Outline each Trypanosoma brucei.
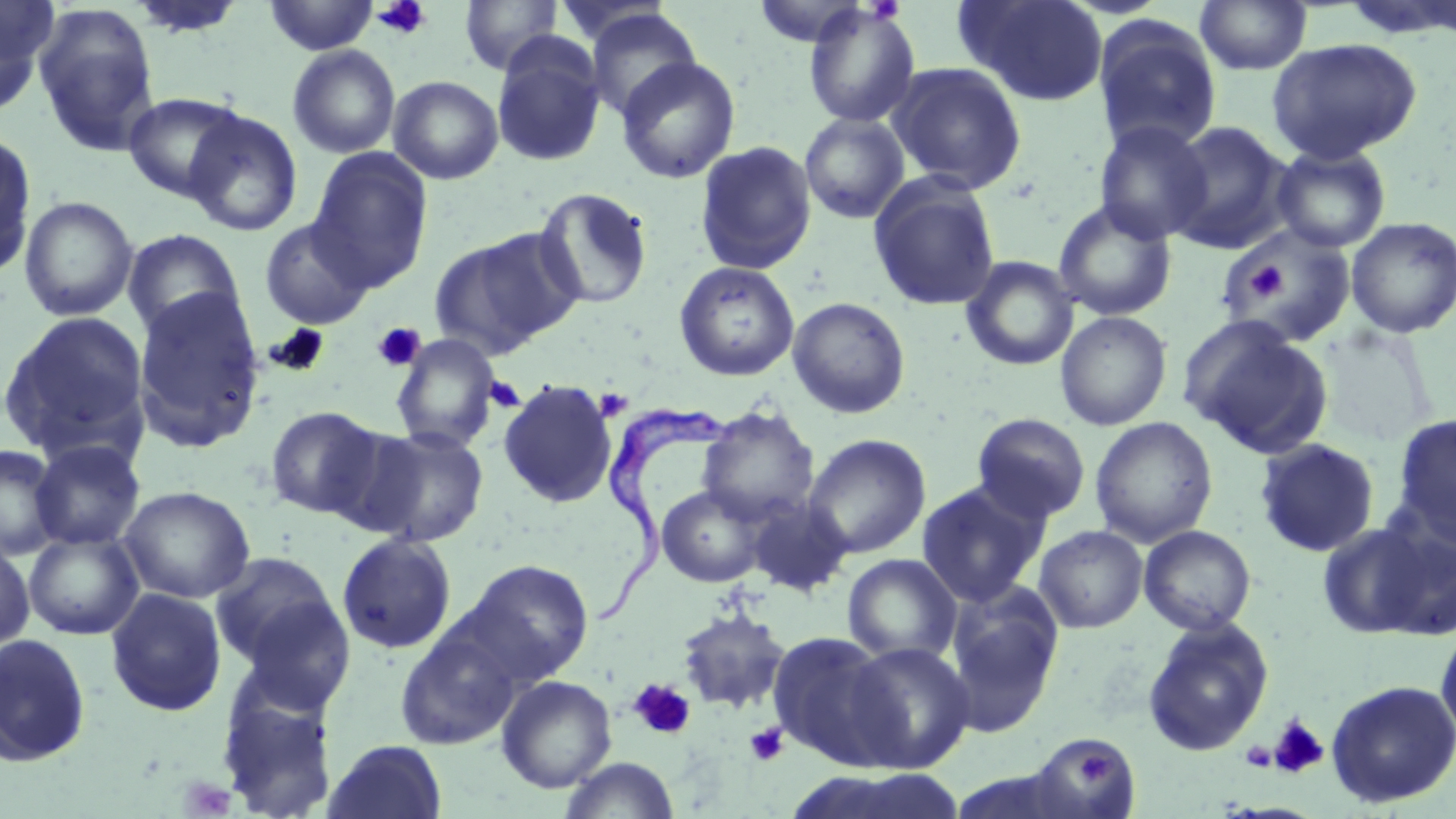
Approximate bounding boxes as (x1,y1)-(x2,y2) corner pairs in pixels.
Trypanosoma brucei: (591,402)-(743,627).

Summary:
  - Uninfected red blood cell locations: (263,0)-(380,56), (459,0)-(563,76), (752,0)-(872,47), (956,0)-(1109,106), (128,1)-(247,40), (1195,1)-(1312,75), (0,2)-(57,115), (32,4)-(161,156), (802,4)-(921,128), (581,8)-(703,121), (1092,14)-(1222,156), (491,36)-(608,167), (1266,38)-(1422,163), (287,44)-(401,159), (615,56)-(741,184), (886,61)-(1028,195), (388,75)-(504,184), (122,92)-(245,202), (183,109)-(302,236), (799,112)-(910,224), (1094,120)-(1214,244), (1162,122)-(1293,252), (0,130)-(38,279), (694,140)-(817,275), (1271,144)-(1391,253), (308,148)-(433,292), (868,175)-(1001,311), (532,186)-(654,310), (18,195)-(139,321), (1053,199)-(1177,321), (1345,217)-(1456,338), (258,218)-(374,329), (1220,225)-(1357,348), (121,228)-(247,343), (429,230)-(581,361), (960,255)-(1080,371), (674,261)-(800,381), (131,288)-(266,452), (787,297)-(910,419), (0,311)-(151,461), (1054,311)-(1172,431), (1181,317)-(1334,458), (1317,326)-(1434,447), (390,334)-(501,453), (497,379)-(618,508), (265,405)-(385,519), (696,406)-(820,526), (971,413)-(1091,524), (1391,414)-(1456,545), (1090,416)-(1218,547), (358,425)-(489,546), (804,434)-(932,559), (1254,438)-(1380,557), (29,439)-(145,551), (0,443)-(64,560), (916,479)-(1051,608), (656,485)-(768,587), (118,486)-(255,603), (745,495)-(853,597), (1315,520)-(1442,640), (1033,525)-(1148,633), (1139,525)-(1256,635), (24,529)-(144,640), (337,532)-(457,655), (0,538)-(35,652), (209,550)-(342,671), (842,554)-(962,665), (462,558)-(594,685), (943,587)-(1064,737), (105,588)-(227,716), (234,595)-(357,715), (675,608)-(790,714), (1141,618)-(1274,756), (1435,622)-(1456,745), (394,625)-(522,750), (767,630)-(902,769), (0,633)-(92,767), (845,640)-(976,773), (496,675)-(617,793), (214,677)-(340,819), (1326,679)-(1456,807), (1028,733)-(1140,818), (323,739)-(448,819), (559,756)-(680,819), (794,769)-(969,819)
  - Platelet locations: (372,0)-(432,39), (1239,257)-(1287,305), (372,323)-(426,372), (482,374)-(527,415), (594,388)-(633,421), (628,678)-(696,740), (1267,715)-(1330,779), (745,723)-(788,767), (1240,741)-(1277,772), (1073,746)-(1114,788)
  - Slide-level diagnosis: Trypanosoma brucei
  - Image size: 1456×819 pixels
  - Modality: optical microscopy
  - Field of view: single
  - Stain: May-Grünwald-Giemsa
  - Magnification: 1000x
  - Preparation: thin blood film